Report the malaria status of this cell.
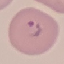

Parasitized.

Photographed with a smartphone camera at the microscope eyepiece. Automatically extracted cell patch, resized to 64 × 64 pixels. Thin smear of blood. Giemsa stain.